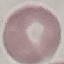
malaria status = uninfected
capture = smartphone through the microscope eyepiece
stain = Giemsa
preparation = thin blood film
image type = cell patch, automatically extracted from a larger field of view and resized to 64 × 64 pixels